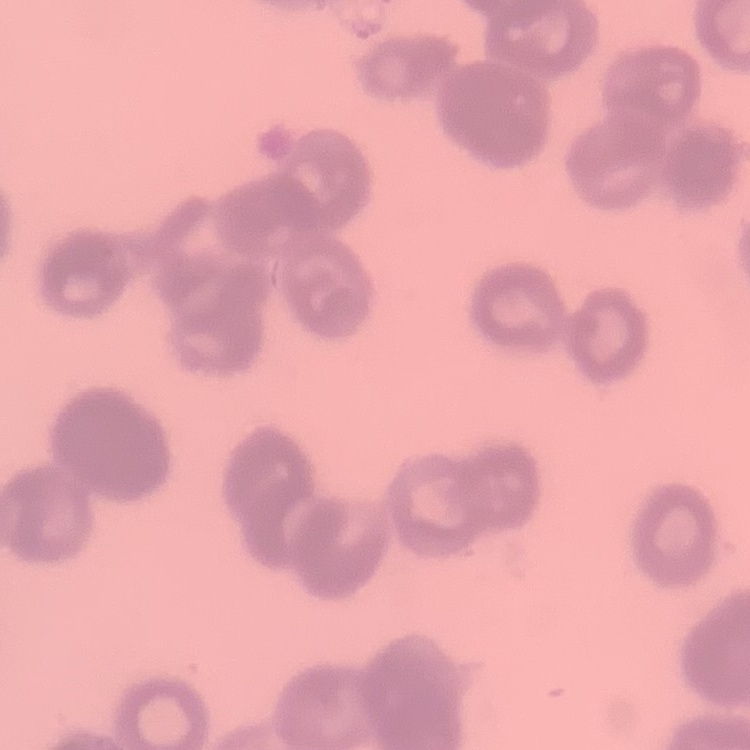
Summary:
  - Erythrocyte morphology: rouleaux formation
  - Preparation: thin peripheral smear
  - Image type: one tile cut from a larger photomicrograph
  - Stain: Field's or Giemsa